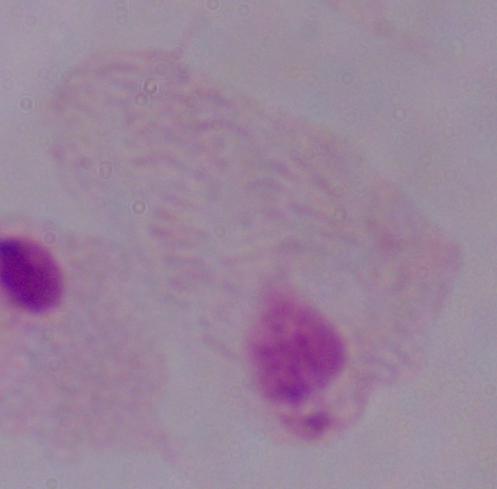
Summary:
  - Magnification: 1000x
  - Modality: photomicrograph
  - Identification: trichomonad